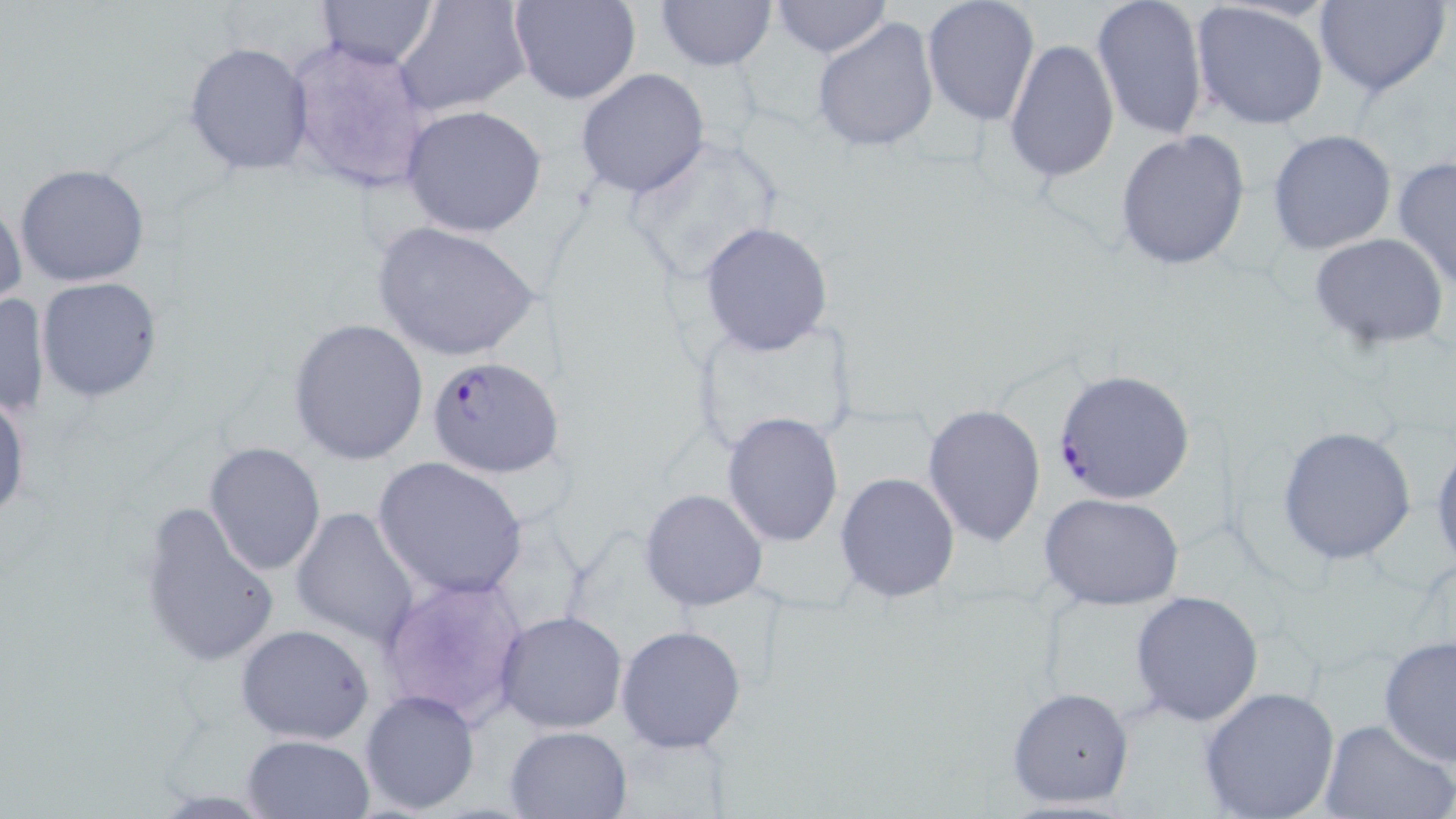

Approximate bounding boxes as named x1/y1/x2/y2 corners in pixels. Plasmodium falciparum-infected red blood cell locations: (x1=429, y1=355, x2=563, y2=478), (x1=1052, y1=368, x2=1194, y2=505). Uninfected red blood cell locations: (x1=317, y1=0, x2=438, y2=69), (x1=508, y1=0, x2=640, y2=104), (x1=922, y1=0, x2=1040, y2=126), (x1=1091, y1=0, x2=1210, y2=143), (x1=1314, y1=0, x2=1451, y2=98), (x1=655, y1=1, x2=776, y2=72), (x1=768, y1=1, x2=893, y2=59), (x1=394, y1=2, x2=530, y2=119), (x1=1189, y1=2, x2=1331, y2=132), (x1=312, y1=16, x2=518, y2=161), (x1=811, y1=16, x2=940, y2=155), (x1=283, y1=35, x2=433, y2=196), (x1=1003, y1=36, x2=1121, y2=183), (x1=184, y1=41, x2=313, y2=175), (x1=575, y1=68, x2=710, y2=199), (x1=399, y1=104, x2=549, y2=238), (x1=1116, y1=128, x2=1251, y2=271), (x1=1267, y1=129, x2=1397, y2=254), (x1=618, y1=132, x2=786, y2=290), (x1=1391, y1=155, x2=1456, y2=291), (x1=14, y1=163, x2=152, y2=287), (x1=0, y1=200, x2=27, y2=313), (x1=372, y1=222, x2=542, y2=363), (x1=698, y1=222, x2=836, y2=359), (x1=1309, y1=233, x2=1450, y2=351), (x1=37, y1=276, x2=163, y2=403), (x1=1, y1=291, x2=51, y2=420), (x1=686, y1=314, x2=861, y2=463), (x1=287, y1=317, x2=430, y2=466), (x1=0, y1=390, x2=30, y2=526), (x1=922, y1=403, x2=1046, y2=547), (x1=721, y1=412, x2=844, y2=547), (x1=1277, y1=425, x2=1419, y2=565), (x1=1430, y1=438, x2=1455, y2=574), (x1=204, y1=440, x2=327, y2=576), (x1=372, y1=456, x2=529, y2=601), (x1=834, y1=472, x2=961, y2=603), (x1=640, y1=489, x2=767, y2=611), (x1=1042, y1=494, x2=1184, y2=609), (x1=137, y1=500, x2=281, y2=671), (x1=290, y1=507, x2=420, y2=645), (x1=1130, y1=590, x2=1264, y2=727), (x1=495, y1=609, x2=628, y2=734), (x1=235, y1=623, x2=375, y2=744), (x1=615, y1=625, x2=747, y2=751), (x1=1378, y1=635, x2=1456, y2=768), (x1=1007, y1=685, x2=1135, y2=811), (x1=1197, y1=685, x2=1340, y2=819), (x1=360, y1=688, x2=480, y2=814), (x1=1317, y1=718, x2=1454, y2=819), (x1=503, y1=725, x2=633, y2=818), (x1=241, y1=733, x2=374, y2=818). Slide-level diagnosis: Plasmodium falciparum. Image is 1456×819 pixels. May-Grünwald-Giemsa-stained preparation. 1000x magnification. Single field of view. Thin blood smear. Light microscopy.